Classify this cell by malaria status.
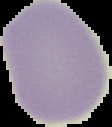

It is uninfected.

Summary:
  - Image size: 112×127 pixels
  - Preparation: thin blood smear
  - Image type: segmented cell region with the area outside set to black